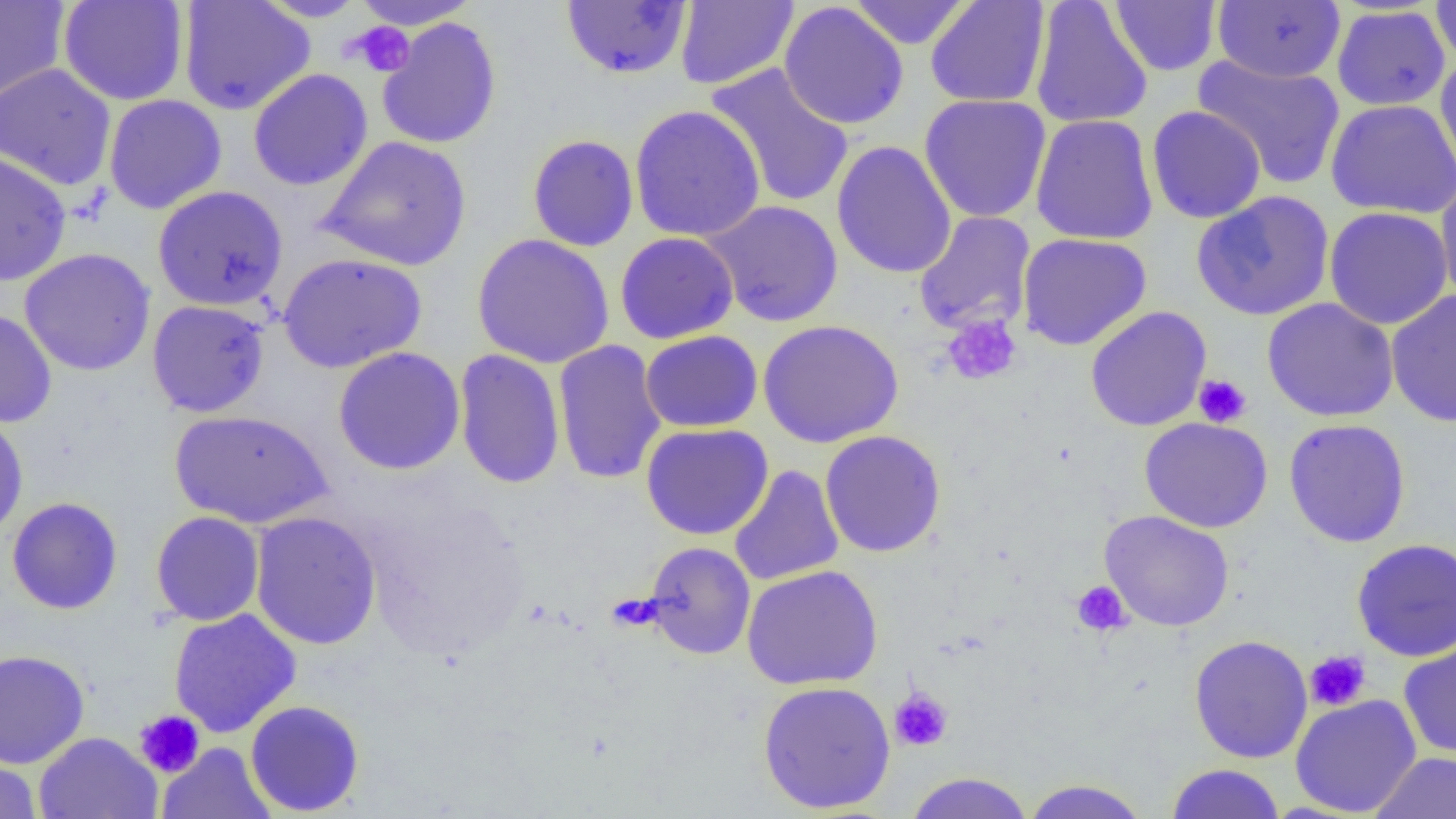
Summary:
  - Coordinate format: approximate bounding boxes as named x1/y1/x2/y2 corners in pixels
  - Uninfected red blood cell locations: (x1=0, y1=0, x2=69, y2=105), (x1=58, y1=0, x2=189, y2=106), (x1=178, y1=0, x2=315, y2=115), (x1=256, y1=0, x2=369, y2=22), (x1=349, y1=0, x2=482, y2=30), (x1=675, y1=0, x2=799, y2=89), (x1=848, y1=0, x2=971, y2=49), (x1=925, y1=0, x2=1050, y2=108), (x1=1030, y1=0, x2=1153, y2=130), (x1=1212, y1=0, x2=1345, y2=83), (x1=1431, y1=0, x2=1456, y2=68), (x1=560, y1=1, x2=692, y2=79), (x1=779, y1=1, x2=909, y2=130), (x1=1109, y1=1, x2=1222, y2=75), (x1=1332, y1=5, x2=1450, y2=111), (x1=377, y1=17, x2=502, y2=150), (x1=1192, y1=53, x2=1346, y2=190), (x1=1434, y1=57, x2=1456, y2=181), (x1=0, y1=62, x2=117, y2=191), (x1=705, y1=62, x2=855, y2=209), (x1=248, y1=69, x2=373, y2=191), (x1=0, y1=81, x2=226, y2=199), (x1=918, y1=93, x2=1052, y2=223), (x1=104, y1=94, x2=227, y2=214), (x1=1325, y1=98, x2=1456, y2=219), (x1=629, y1=104, x2=766, y2=243), (x1=1146, y1=105, x2=1266, y2=224), (x1=1030, y1=114, x2=1159, y2=245), (x1=527, y1=134, x2=640, y2=252), (x1=315, y1=135, x2=473, y2=272), (x1=831, y1=140, x2=957, y2=279), (x1=0, y1=150, x2=71, y2=287), (x1=1436, y1=176, x2=1456, y2=308), (x1=153, y1=184, x2=289, y2=311), (x1=1191, y1=191, x2=1335, y2=321), (x1=703, y1=200, x2=844, y2=327), (x1=1324, y1=206, x2=1453, y2=329), (x1=914, y1=212, x2=1036, y2=336), (x1=615, y1=231, x2=739, y2=344), (x1=1017, y1=232, x2=1152, y2=351), (x1=471, y1=233, x2=615, y2=369), (x1=19, y1=248, x2=156, y2=376), (x1=277, y1=252, x2=428, y2=374), (x1=1386, y1=289, x2=1456, y2=428), (x1=1262, y1=297, x2=1400, y2=422), (x1=147, y1=300, x2=270, y2=417), (x1=1085, y1=306, x2=1212, y2=432), (x1=0, y1=308, x2=57, y2=428), (x1=758, y1=319, x2=904, y2=448), (x1=639, y1=329, x2=763, y2=433), (x1=552, y1=339, x2=667, y2=485), (x1=333, y1=346, x2=466, y2=475), (x1=453, y1=349, x2=566, y2=489), (x1=0, y1=409, x2=29, y2=541), (x1=170, y1=409, x2=333, y2=528), (x1=1139, y1=416, x2=1273, y2=533), (x1=1284, y1=418, x2=1411, y2=547), (x1=641, y1=423, x2=773, y2=540), (x1=819, y1=429, x2=946, y2=557), (x1=728, y1=464, x2=844, y2=587), (x1=7, y1=497, x2=123, y2=615), (x1=1099, y1=509, x2=1235, y2=632), (x1=151, y1=511, x2=265, y2=626), (x1=249, y1=511, x2=382, y2=650), (x1=1351, y1=537, x2=1456, y2=662), (x1=642, y1=541, x2=756, y2=659), (x1=742, y1=564, x2=883, y2=690), (x1=168, y1=608, x2=302, y2=738), (x1=1189, y1=635, x2=1313, y2=763), (x1=1398, y1=638, x2=1456, y2=760), (x1=0, y1=649, x2=90, y2=769), (x1=757, y1=680, x2=896, y2=813), (x1=1290, y1=694, x2=1422, y2=817), (x1=245, y1=699, x2=365, y2=816), (x1=33, y1=731, x2=162, y2=819), (x1=157, y1=742, x2=276, y2=819), (x1=1369, y1=751, x2=1456, y2=818), (x1=0, y1=757, x2=42, y2=819), (x1=1164, y1=763, x2=1286, y2=819), (x1=904, y1=772, x2=1034, y2=819), (x1=1017, y1=779, x2=1153, y2=819)
  - Platelet locations: (x1=348, y1=21, x2=415, y2=77), (x1=942, y1=313, x2=1022, y2=385), (x1=1193, y1=374, x2=1252, y2=428), (x1=1071, y1=581, x2=1131, y2=637), (x1=1304, y1=650, x2=1371, y2=712), (x1=888, y1=688, x2=953, y2=752), (x1=134, y1=710, x2=205, y2=778)
  - Slide-level diagnosis: no evidence of blood parasites
  - Preparation: thin blood film
  - Modality: light microscopy
  - Magnification: 1000x
  - Field of view: one of a larger specimen
  - Image size: 1456×819 pixels